Identify the parasite.
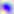

This is Toxoplasma gondii.

Summary:
  - Magnification: 400x
  - Modality: photomicrograph